Comment on the morphology of the red blood cells.
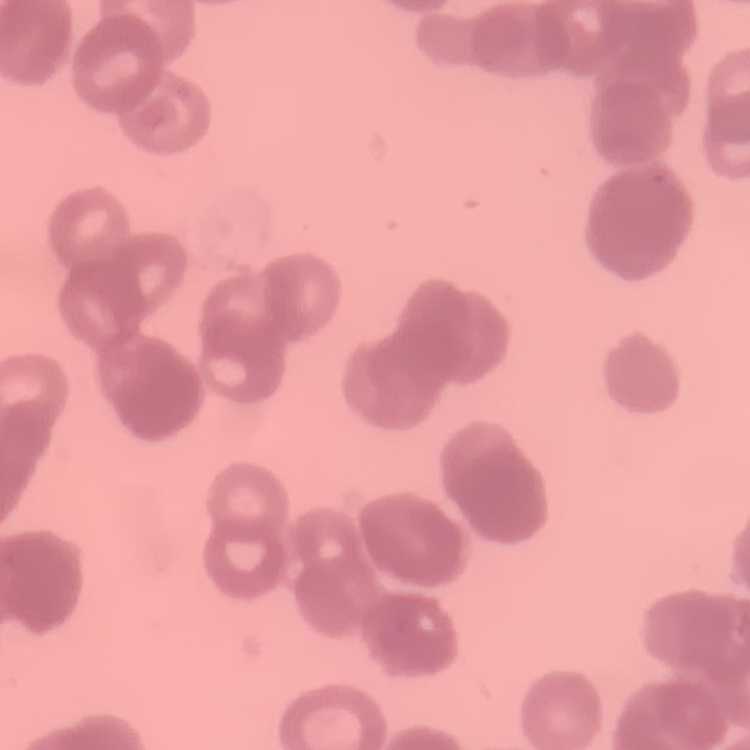

Rouleaux formation.

Stained with either Field's or Giemsa. Square crop of a larger photomicrograph. Thin blood smear.